Evaluate for Plasmodium parasites.
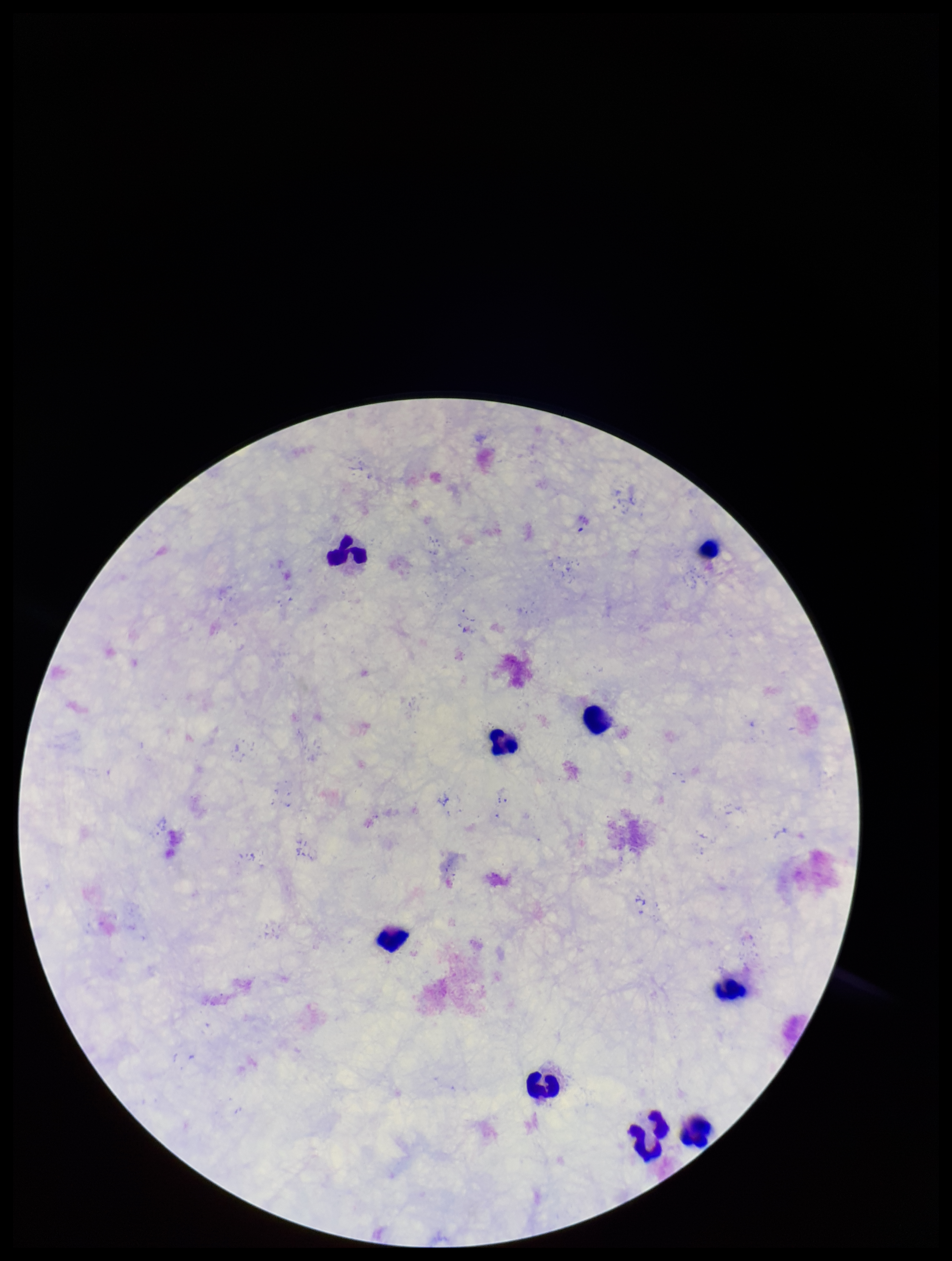

None seen.

Single field of view. Giemsa stain. Leukocyte count: 9. Patient malaria status: negative. Preparation: thick blood smear. Parasite count: 0. Photographed through the microscope eyepiece with a smartphone camera. Image is 952×1261 pixels.